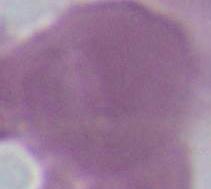

Summary:
  - Magnification: 1000x
  - Identification: erythrocyte
  - Modality: photomicrograph